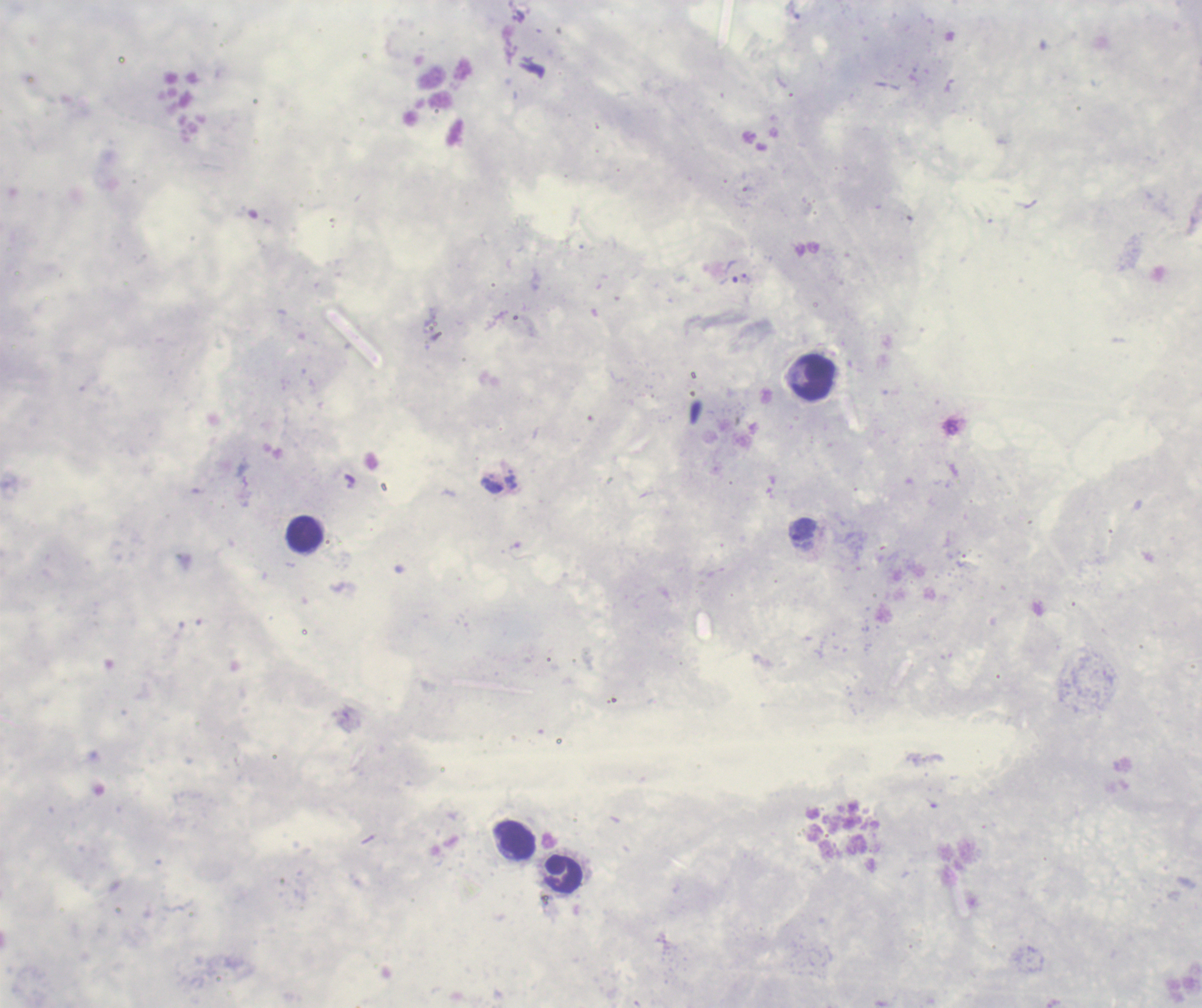
{
  "leukocyte_locations": "approximate centers as [x, y] in pixels: [813, 378], [305, 535], [515, 841], [563, 875]",
  "field_of_view": "one from this slide",
  "magnification": "100x",
  "stain": "Romanowsky",
  "result": "positive for malaria parasites",
  "preparation": "thick blood film",
  "trophozoite_locations": "approximate centers as [x, y] in pixels: [732, 271], [804, 530]",
  "background_quality": "unsatisfactory",
  "context": "previously used in a real diagnosis",
  "image_size": "1202×1008 pixels"
}